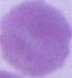

Summary:
  - Identification: erythrocyte
  - Magnification: 1000x
  - Modality: micrograph